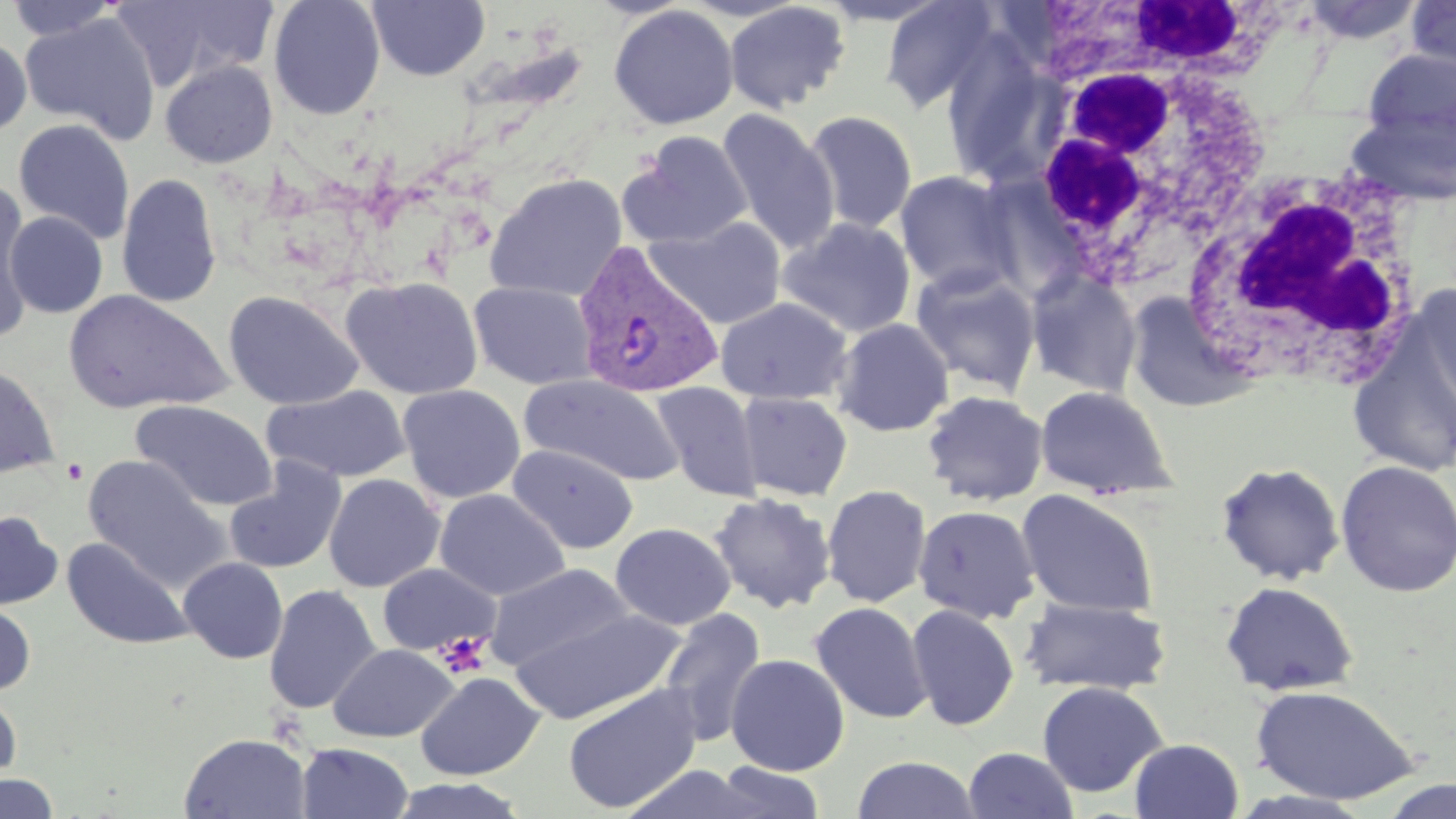

Approximate bounding boxes as [x1, y1, x2, y2] in pixels. Uninfected red blood cell locations: [5, 0, 123, 41], [111, 0, 279, 91], [268, 0, 385, 119], [366, 0, 490, 82], [816, 0, 953, 27], [879, 0, 1000, 113], [1404, 0, 1456, 82], [724, 1, 851, 113], [609, 4, 738, 130], [19, 12, 161, 144], [0, 35, 32, 138], [941, 35, 1061, 187], [1360, 47, 1456, 151], [160, 60, 278, 168], [716, 108, 839, 254], [1343, 108, 1456, 206], [804, 111, 918, 234], [13, 118, 135, 245], [622, 131, 754, 249], [895, 170, 1022, 297], [116, 173, 222, 308], [485, 173, 627, 302], [0, 188, 35, 335], [4, 211, 108, 318], [648, 216, 786, 329], [779, 217, 915, 338], [910, 264, 1042, 400], [1025, 270, 1142, 397], [341, 276, 484, 399], [468, 280, 597, 390], [1411, 283, 1455, 416], [62, 290, 232, 414], [223, 290, 364, 410], [715, 297, 852, 405], [832, 318, 955, 436], [1347, 321, 1456, 479], [0, 363, 60, 478], [519, 373, 684, 486], [651, 381, 764, 501], [397, 384, 525, 504], [1036, 384, 1175, 499], [263, 385, 411, 482], [921, 389, 1048, 506], [736, 391, 853, 501], [131, 400, 278, 510], [507, 443, 639, 554], [83, 454, 229, 592], [224, 459, 346, 575], [1335, 459, 1456, 598], [1215, 462, 1346, 585], [323, 473, 445, 592], [822, 484, 931, 607], [434, 488, 570, 601], [1016, 489, 1158, 617], [709, 492, 837, 614], [913, 504, 1041, 624], [0, 510, 64, 610], [610, 522, 735, 630], [62, 536, 192, 650], [178, 557, 288, 663], [377, 562, 501, 657], [485, 562, 634, 671], [1219, 580, 1360, 697], [263, 584, 381, 714], [1019, 597, 1171, 695], [0, 601, 36, 696], [809, 601, 932, 724], [907, 604, 1019, 731], [509, 606, 685, 724], [658, 607, 766, 746], [328, 643, 459, 742], [725, 653, 849, 776], [415, 671, 545, 781], [1037, 680, 1168, 797], [562, 683, 704, 814], [1249, 683, 1423, 806], [0, 688, 22, 784], [179, 732, 311, 818], [1129, 738, 1243, 819], [296, 743, 414, 819], [962, 747, 1079, 819], [851, 755, 982, 818], [710, 761, 827, 819], [0, 773, 59, 818], [386, 777, 530, 819]. White blood cell locations: [1046, 0, 1306, 86], [1021, 47, 1270, 288], [1177, 158, 1433, 395]. Platelet locations: [63, 458, 89, 484], [433, 632, 492, 680]. Plasmodium vivax-infected red blood cell locations: [572, 242, 725, 400]. Slide-level diagnosis: Plasmodium vivax. May-Grünwald-Giemsa stain. Single field of view. Image is 1456×819 pixels. Thin blood film. Optical microscopy. 1000x magnification.